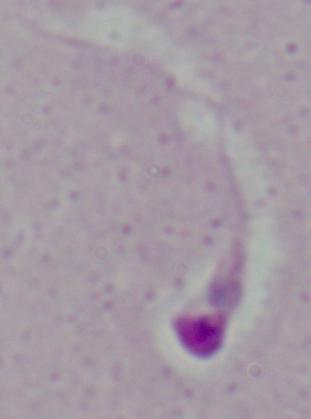

magnification: 1000x
identification: Leishmania
modality: micrograph